Locate every malaria parasite and every leukocyte.
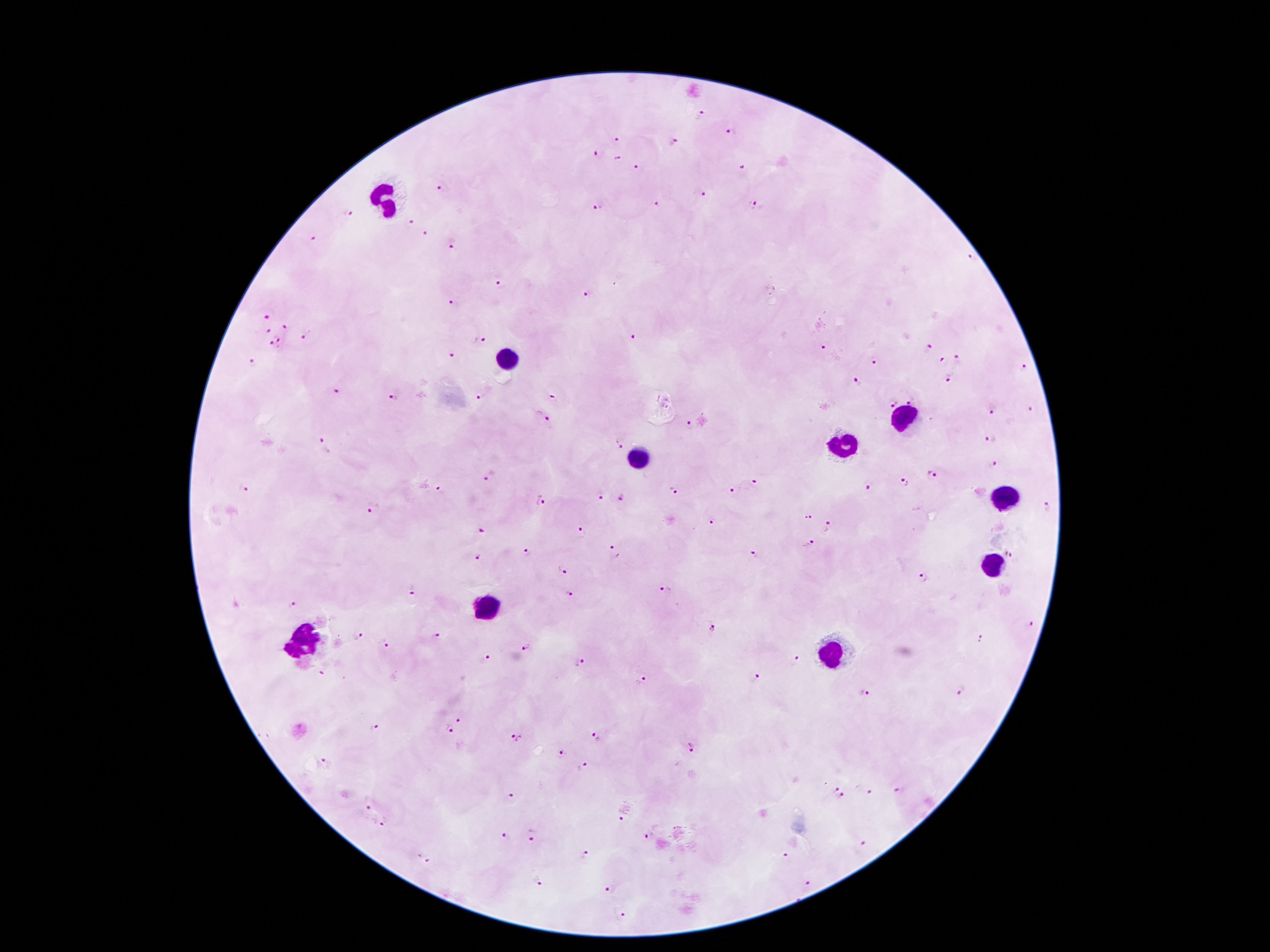
Approximate centers as {x, y} in pixels.
Malaria parasites: {701, 115}, {731, 132}, {616, 141}, {675, 141}, {598, 154}, {617, 159}, {637, 168}, {743, 169}, {443, 188}, {701, 196}, {656, 203}, {752, 205}, {597, 206}, {348, 214}, {412, 221}, {427, 235}, {313, 239}, {452, 243}, {500, 284}, {588, 295}, {449, 302}, {267, 316}, {285, 328}, {267, 330}, {634, 336}, {278, 338}, {303, 338}, {480, 340}, {273, 345}, {823, 348}, {928, 348}, {452, 356}, {959, 358}, {942, 359}, {873, 362}, {252, 363}, {1023, 368}, {948, 377}, {858, 383}, {335, 393}, {393, 398}, {551, 398}, {480, 399}, {910, 401}, {892, 403}, {1030, 410}, {992, 412}, {543, 415}, {690, 425}, {990, 438}, {321, 441}, {619, 443}, {993, 465}, {932, 473}, {491, 475}, {753, 483}, {904, 483}, {867, 488}, {440, 489}, {246, 490}, {733, 490}, {672, 491}, {600, 498}, {623, 498}, {540, 501}, {1046, 506}, {372, 511}, {808, 516}, {713, 522}, {829, 528}, {481, 532}, {582, 532}, {809, 544}, {613, 548}, {528, 553}, {1011, 553}, {753, 555}, {479, 557}, {561, 573}, {923, 576}, {414, 590}, {666, 591}, {569, 593}, {292, 604}, {1030, 624}, {710, 629}, {359, 635}, {435, 636}, {981, 640}, {384, 643}, {525, 647}, {488, 657}, {793, 659}, {580, 662}, {322, 673}, {756, 678}, {643, 682}, {961, 691}, {865, 695}, {459, 723}, {375, 729}, {449, 731}, {597, 736}, {517, 739}, {691, 746}, {562, 755}, {325, 761}, {585, 767}, {837, 789}, {899, 791}, {871, 794}, {510, 797}, {843, 797}, {368, 807}, {622, 819}, {383, 823}, {505, 835}, {532, 837}, {647, 837}, {863, 843}, {586, 855}, {788, 856}, {425, 859}, {538, 881}, {810, 885}, {611, 888}, {624, 916}.
Leukocytes: {384, 197}, {508, 360}, {902, 419}, {842, 447}, {638, 459}, {1005, 497}, {993, 567}, {491, 606}, {302, 642}, {829, 653}.

magnification = 100x
stain = Giemsa
field of view = one from this slide
patient malaria status = positive for Plasmodium falciparum
capture = smartphone camera through the microscope eyepiece
preparation = thick blood film
image size = 1270×952 pixels